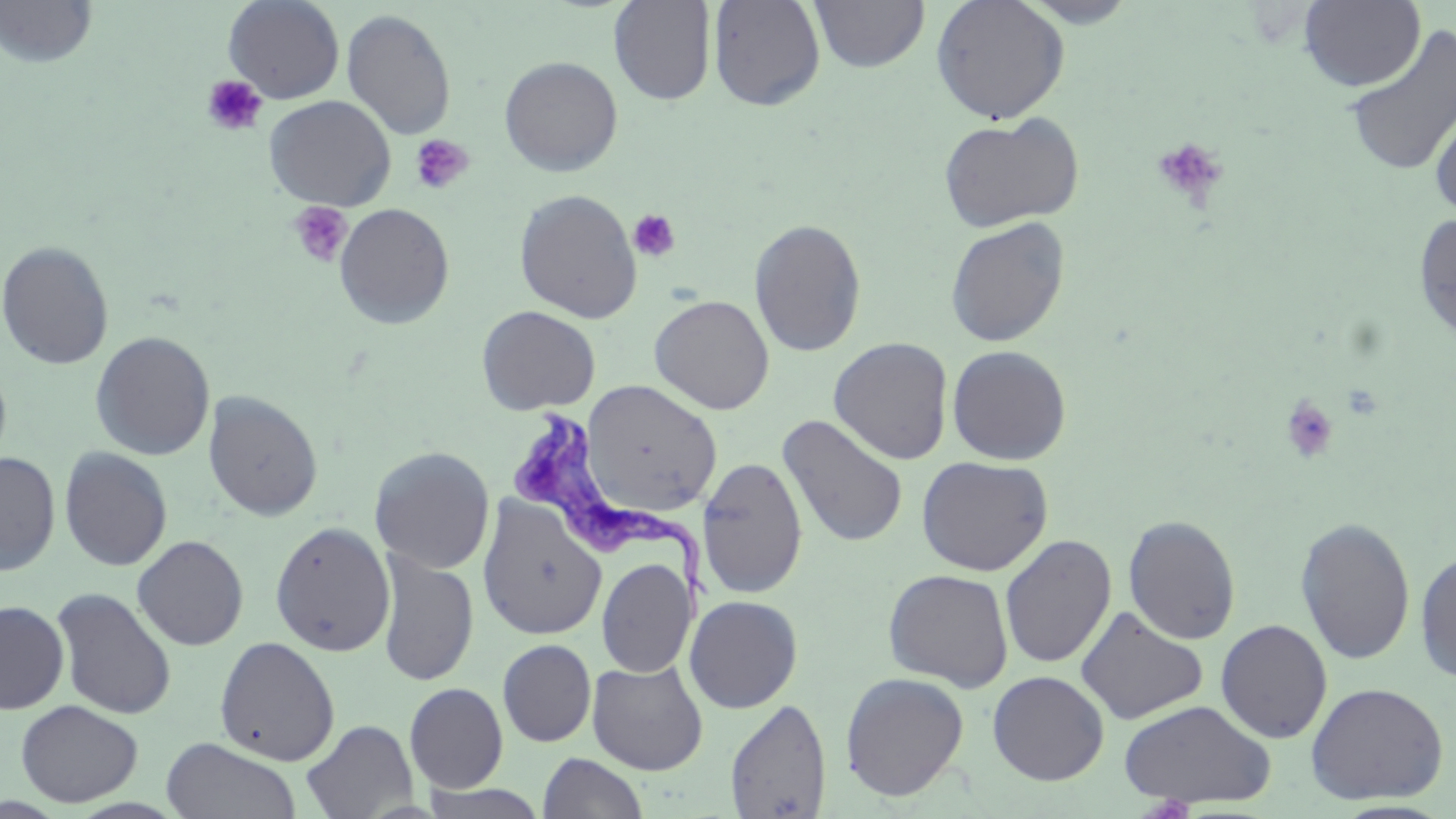
slide-level diagnosis = Trypanosoma brucei
uninfected red blood cell locations = approximate bounding boxes as (x1, y1, x2, y2) in pixels: (1, 0, 99, 68), (224, 0, 345, 104), (707, 0, 826, 111), (809, 0, 930, 73), (930, 0, 1070, 124), (1018, 0, 1141, 28), (1298, 0, 1425, 91), (608, 1, 716, 105), (341, 8, 457, 140), (1342, 23, 1456, 179), (499, 56, 623, 176), (264, 95, 396, 210), (1429, 100, 1456, 219), (938, 114, 1084, 232), (514, 189, 643, 323), (333, 202, 455, 330), (1412, 213, 1456, 344), (944, 216, 1070, 348), (749, 218, 867, 357), (0, 240, 114, 370), (649, 295, 774, 414), (477, 305, 600, 415), (90, 331, 215, 460), (829, 337, 953, 465), (946, 344, 1072, 465), (575, 380, 723, 517), (203, 390, 323, 522), (777, 414, 909, 548), (370, 446, 495, 574), (58, 447, 173, 572), (0, 451, 60, 576), (916, 455, 1053, 576), (697, 457, 808, 599), (477, 497, 607, 641), (1123, 514, 1241, 645), (1295, 516, 1416, 666), (270, 521, 395, 657), (999, 534, 1116, 669), (132, 535, 248, 650), (1414, 547, 1456, 684), (376, 550, 479, 687), (596, 558, 696, 678), (883, 568, 1014, 691), (50, 587, 177, 720), (684, 594, 803, 713), (0, 600, 70, 714), (1075, 606, 1208, 724), (1215, 619, 1332, 743), (214, 635, 340, 766), (498, 639, 596, 747), (586, 659, 709, 775), (987, 671, 1109, 785), (840, 672, 969, 801), (404, 681, 509, 792), (1305, 681, 1449, 804), (725, 698, 831, 818), (1119, 698, 1277, 808), (16, 700, 143, 807), (301, 718, 418, 818), (161, 737, 302, 819), (538, 752, 649, 818), (418, 782, 551, 818)
modality = optical microscopy
field of view = single
image size = 1456×819 pixels
stain = May-Grünwald-Giemsa
preparation = thin blood film
Trypanosoma brucei locations = approximate bounding boxes as (x1, y1, x2, y2) in pixels: (510, 409, 721, 602)
platelet locations = approximate bounding boxes as (x1, y1, x2, y2) in pixels: (201, 74, 268, 136), (410, 133, 474, 194), (1152, 137, 1228, 206), (287, 201, 353, 268), (627, 209, 681, 262), (1280, 395, 1339, 465)
magnification = 1000x